Point out each Plasmodium parasite.
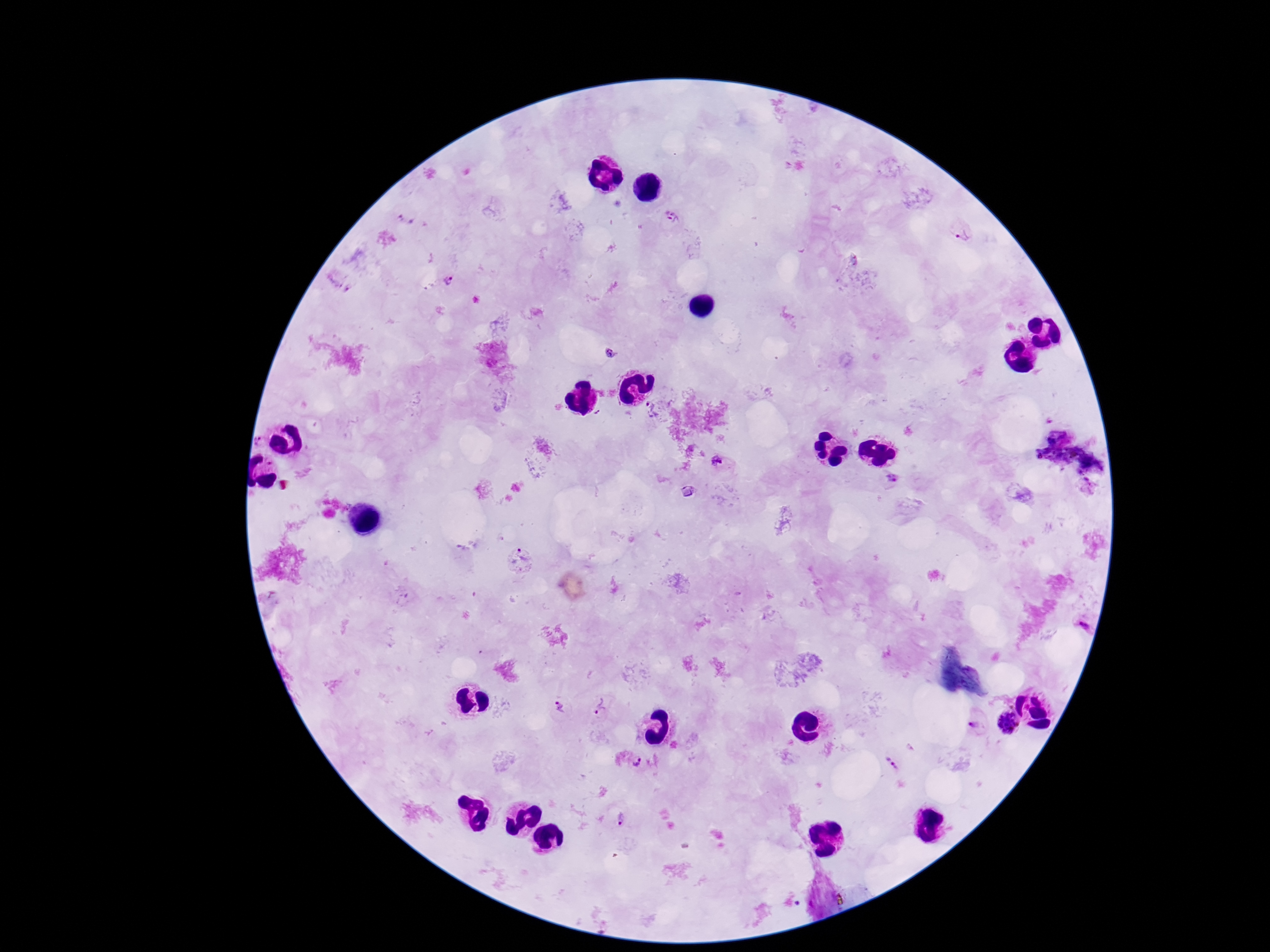
Approximate object centers, in pixels from the top-left corner.
Plasmodium parasites: (x=673, y=218), (x=406, y=220), (x=960, y=232), (x=448, y=278), (x=611, y=354), (x=652, y=408), (x=259, y=441), (x=717, y=461), (x=894, y=480), (x=520, y=559), (x=1083, y=624), (x=560, y=707), (x=601, y=708), (x=1006, y=722), (x=974, y=725), (x=635, y=760), (x=893, y=762), (x=620, y=818).

image size = 1270×952 pixels
preparation = thick blood film
magnification = 100x
patient malaria status = positive
field of view = single
stain = Giemsa
capture = smartphone camera through the microscope eyepiece